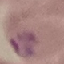

Summary:
  - Result: malaria parasites identified
  - Preparation: thin blood film
  - Capture: smartphone through the microscope eyepiece
  - Image type: cell patch, automatically extracted from a larger field of view and resized to 64 × 64 pixels
  - Stain: Giemsa